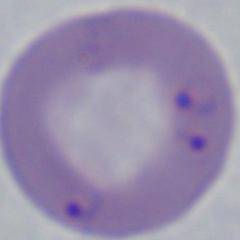

A Babesia parasite is seen. Photomicrograph. 1000x magnification.